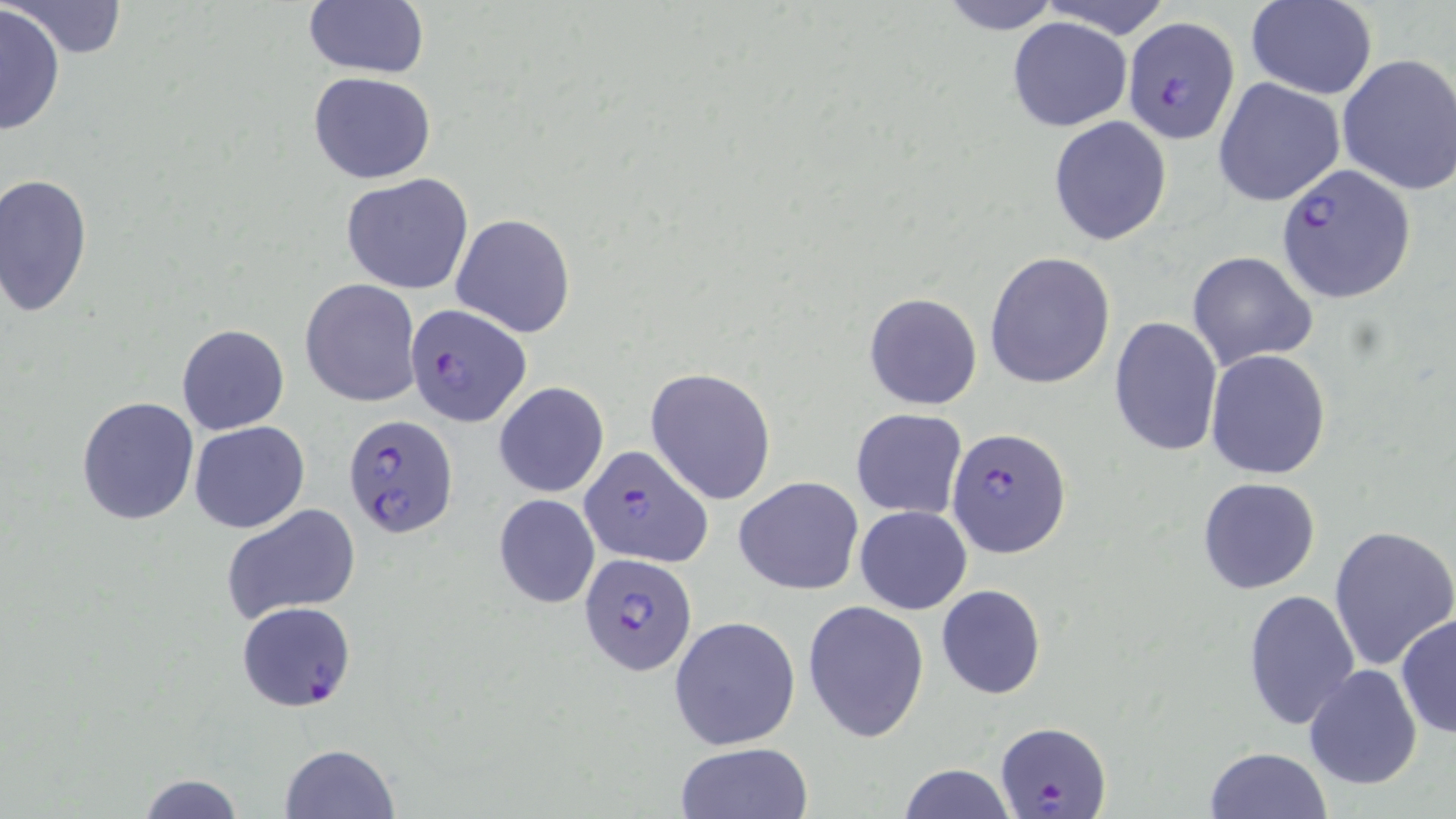
slide-level diagnosis = Plasmodium falciparum
stain = May-Grünwald-Giemsa
modality = light microscopy
preparation = thin blood film
image size = 1456×819 pixels
Plasmodium falciparum-infected red blood cell locations = approximate bounding boxes as (x1, y1, x2, y2) in pixels: (1121, 16, 1242, 145), (1275, 164, 1415, 304), (405, 302, 531, 428), (342, 412, 459, 541), (946, 428, 1072, 559), (577, 444, 711, 568), (578, 552, 696, 677), (236, 601, 358, 713), (995, 721, 1112, 816)
magnification = 1000x
field of view = one of a larger specimen
uninfected red blood cell locations = approximate bounding boxes as (x1, y1, x2, y2) in pixels: (10, 0, 131, 59), (935, 0, 1065, 35), (1039, 0, 1176, 40), (1247, 0, 1376, 99), (303, 1, 430, 79), (1, 6, 67, 135), (1007, 17, 1133, 131), (1335, 53, 1455, 196), (308, 72, 437, 184), (1213, 77, 1345, 208), (1050, 107, 1176, 239), (0, 172, 93, 318), (341, 173, 474, 296), (451, 212, 577, 339), (1187, 250, 1316, 372), (985, 253, 1115, 390), (301, 279, 419, 406), (863, 292, 982, 409), (1109, 315, 1225, 458), (177, 323, 289, 434), (1206, 349, 1332, 480), (646, 367, 777, 505), (494, 381, 610, 498), (76, 395, 199, 524), (850, 408, 967, 519), (189, 421, 309, 534), (734, 476, 864, 596), (1197, 476, 1322, 595), (493, 493, 600, 609), (222, 503, 363, 622), (855, 505, 971, 614), (1329, 524, 1456, 670), (935, 585, 1046, 700), (1242, 589, 1360, 731), (802, 601, 930, 743), (1395, 613, 1456, 743), (668, 615, 801, 749), (1303, 663, 1422, 789), (280, 742, 398, 818), (675, 743, 813, 819), (1204, 744, 1334, 818), (914, 750, 1127, 819), (896, 763, 1017, 819), (138, 773, 246, 818)